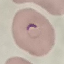
malaria_status: parasitized
stain: Giemsa
preparation: thin blood smear
capture: smartphone camera at the microscope eyepiece
image_type: cell patch, automatically extracted from a larger field of view and resized to 64 × 64 pixels